Identify the blood parasite species.
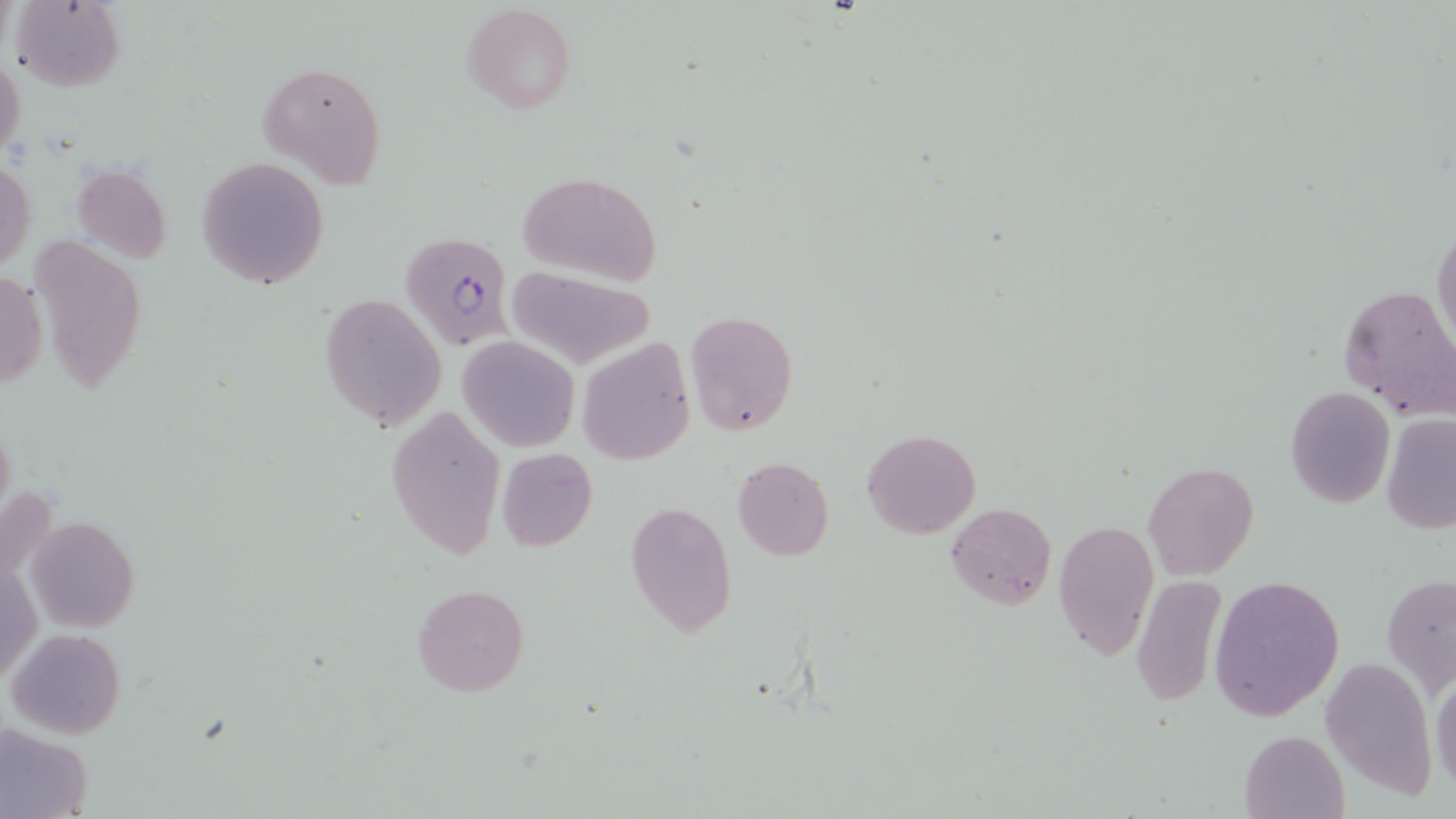
Plasmodium falciparum.

image size = 1456×819 pixels
field of view = one of a larger specimen
stain = May-Grünwald-Giemsa
preparation = thin blood film
Plasmodium falciparum-infected red blood cell locations = approximate bounding boxes as (x1, y1, x2, y2) in pixels: (400, 230, 515, 350)
modality = light microscopy
magnification = 1000x
uninfected red blood cell locations = approximate bounding boxes as (x1, y1, x2, y2) in pixels: (9, 0, 125, 92), (462, 3, 577, 115), (0, 54, 25, 163), (256, 61, 387, 187), (196, 156, 329, 288), (1, 160, 35, 272), (73, 163, 171, 262), (516, 169, 663, 285), (1431, 219, 1456, 354), (27, 232, 148, 392), (504, 267, 657, 370), (1, 271, 47, 390), (1336, 284, 1455, 419), (320, 293, 447, 431), (683, 310, 799, 437), (456, 336, 580, 453), (578, 338, 694, 466), (1285, 387, 1396, 510), (386, 404, 504, 559), (1380, 414, 1455, 534), (862, 428, 980, 538), (495, 449, 598, 552), (731, 456, 835, 560), (1142, 461, 1260, 581), (624, 502, 736, 636), (945, 502, 1056, 608), (23, 514, 139, 633), (1052, 518, 1158, 662), (1, 556, 42, 686), (1382, 572, 1456, 695), (1208, 574, 1345, 721), (1130, 577, 1227, 705), (412, 584, 528, 697), (5, 627, 126, 739), (1321, 654, 1437, 800), (1431, 675, 1456, 792), (0, 724, 92, 819), (1240, 729, 1348, 818)